Outline each blood parasite and name the species.
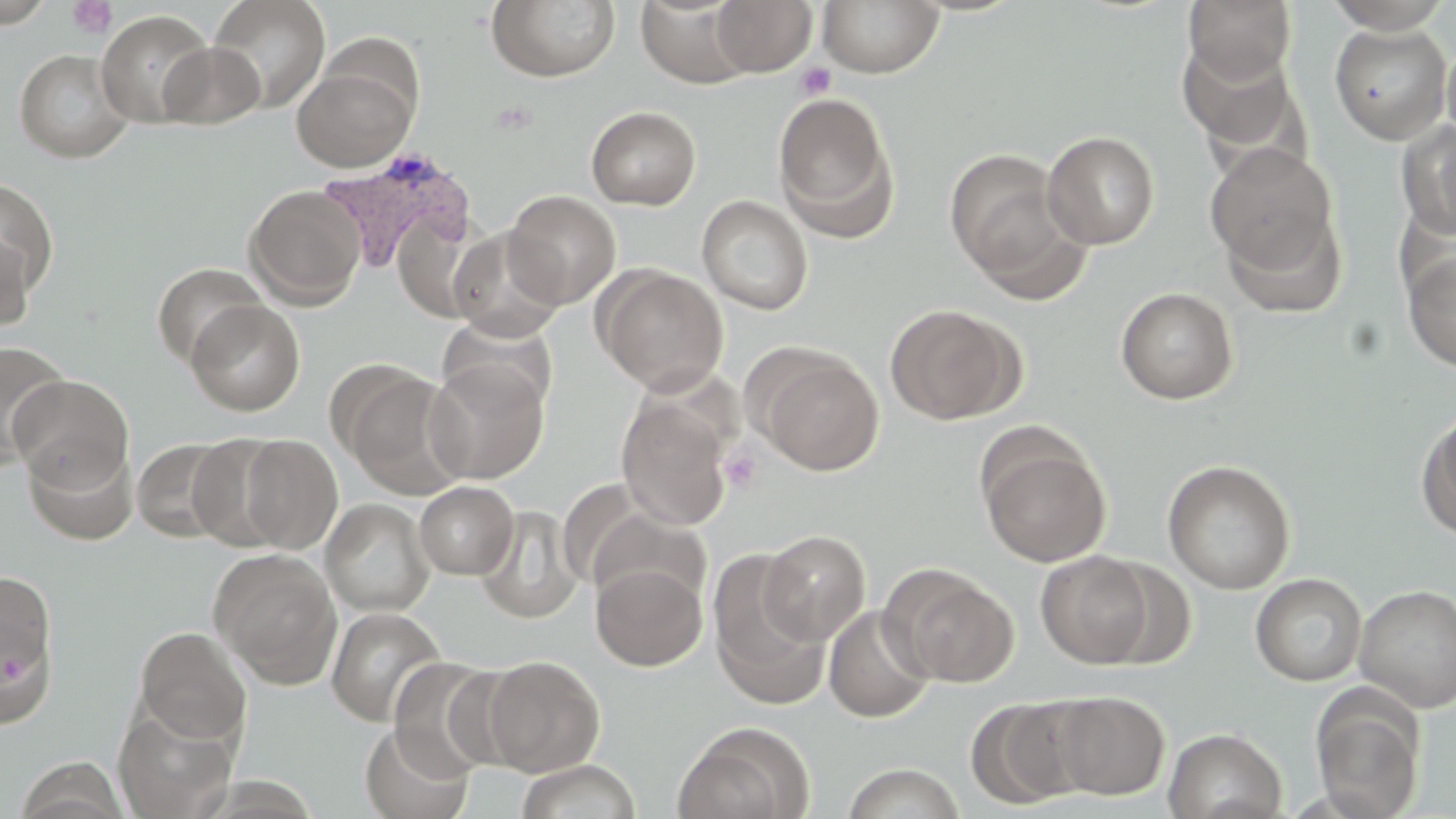

Approximate bounding boxes as named x1/y1/x2/y2 corners in pixels.
Plasmodium vivax-infected red blood cells: (x1=314, y1=150, x2=475, y2=275).
No Plasmodium falciparum, Plasmodium ovale, Plasmodium malariae, Babesia divergens, or Trypanosoma brucei observed.

{
  "slide_level_diagnosis": "Plasmodium vivax",
  "platelet_locations": "approximate bounding boxes as named x1/y1/x2/y2 corners in pixels: (x1=66, y1=1, x2=117, y2=39), (x1=795, y1=62, x2=836, y2=100), (x1=720, y1=445, x2=764, y2=494)",
  "preparation": "thin blood smear",
  "image_size": "1456×819 pixels",
  "modality": "light microscopy",
  "stain": "May-Grünwald-Giemsa",
  "field_of_view": "single",
  "uninfected_red_blood_cell_locations": "approximate bounding boxes as named x1/y1/x2/y2 corners in pixels: (x1=1, y1=0, x2=54, y2=27), (x1=208, y1=0, x2=331, y2=113), (x1=636, y1=0, x2=752, y2=88), (x1=710, y1=0, x2=817, y2=76), (x1=1184, y1=0, x2=1297, y2=84), (x1=1321, y1=0, x2=1454, y2=32), (x1=486, y1=1, x2=621, y2=83), (x1=819, y1=1, x2=944, y2=78), (x1=96, y1=9, x2=216, y2=128), (x1=1329, y1=23, x2=1453, y2=144), (x1=1177, y1=38, x2=1305, y2=158), (x1=1441, y1=38, x2=1456, y2=150), (x1=158, y1=41, x2=265, y2=129), (x1=14, y1=49, x2=135, y2=163), (x1=291, y1=59, x2=417, y2=172), (x1=772, y1=91, x2=899, y2=241), (x1=586, y1=106, x2=701, y2=210), (x1=1399, y1=120, x2=1456, y2=240), (x1=1042, y1=131, x2=1160, y2=249), (x1=1206, y1=144, x2=1340, y2=279), (x1=944, y1=149, x2=1079, y2=291), (x1=0, y1=176, x2=59, y2=302), (x1=243, y1=184, x2=366, y2=309), (x1=502, y1=190, x2=621, y2=308), (x1=697, y1=195, x2=813, y2=316), (x1=1221, y1=204, x2=1347, y2=317), (x1=392, y1=212, x2=491, y2=324), (x1=0, y1=225, x2=35, y2=332), (x1=447, y1=227, x2=567, y2=342), (x1=1403, y1=251, x2=1456, y2=372), (x1=152, y1=262, x2=267, y2=370), (x1=595, y1=266, x2=729, y2=395), (x1=1116, y1=287, x2=1239, y2=405), (x1=186, y1=299, x2=305, y2=416), (x1=884, y1=303, x2=1021, y2=425), (x1=438, y1=316, x2=559, y2=416), (x1=0, y1=340, x2=71, y2=470), (x1=753, y1=349, x2=885, y2=475), (x1=423, y1=359, x2=550, y2=486), (x1=333, y1=363, x2=469, y2=498), (x1=8, y1=373, x2=134, y2=489), (x1=616, y1=392, x2=735, y2=532), (x1=1416, y1=405, x2=1456, y2=541), (x1=977, y1=432, x2=1113, y2=567), (x1=231, y1=433, x2=343, y2=554), (x1=131, y1=436, x2=240, y2=543), (x1=24, y1=438, x2=138, y2=546), (x1=1162, y1=459, x2=1296, y2=594), (x1=415, y1=481, x2=518, y2=580), (x1=320, y1=498, x2=435, y2=616), (x1=474, y1=505, x2=583, y2=624), (x1=759, y1=529, x2=871, y2=645), (x1=208, y1=548, x2=342, y2=689), (x1=708, y1=548, x2=829, y2=705), (x1=1036, y1=550, x2=1156, y2=668), (x1=1094, y1=559, x2=1196, y2=669), (x1=591, y1=562, x2=707, y2=671), (x1=880, y1=564, x2=1019, y2=688), (x1=0, y1=567, x2=60, y2=714), (x1=1250, y1=573, x2=1367, y2=686), (x1=1354, y1=584, x2=1456, y2=713), (x1=823, y1=605, x2=935, y2=723), (x1=325, y1=607, x2=447, y2=727), (x1=134, y1=626, x2=252, y2=746), (x1=480, y1=655, x2=605, y2=775), (x1=386, y1=656, x2=509, y2=779), (x1=1310, y1=689, x2=1426, y2=819), (x1=1048, y1=691, x2=1170, y2=800), (x1=966, y1=695, x2=1091, y2=810), (x1=113, y1=705, x2=239, y2=819), (x1=358, y1=722, x2=474, y2=819), (x1=672, y1=722, x2=813, y2=819), (x1=1163, y1=727, x2=1287, y2=819), (x1=14, y1=757, x2=130, y2=819), (x1=514, y1=759, x2=642, y2=819), (x1=842, y1=762, x2=966, y2=819)",
  "magnification": "1000x"
}